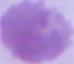
modality = micrograph
identification = erythrocyte
magnification = 1000x